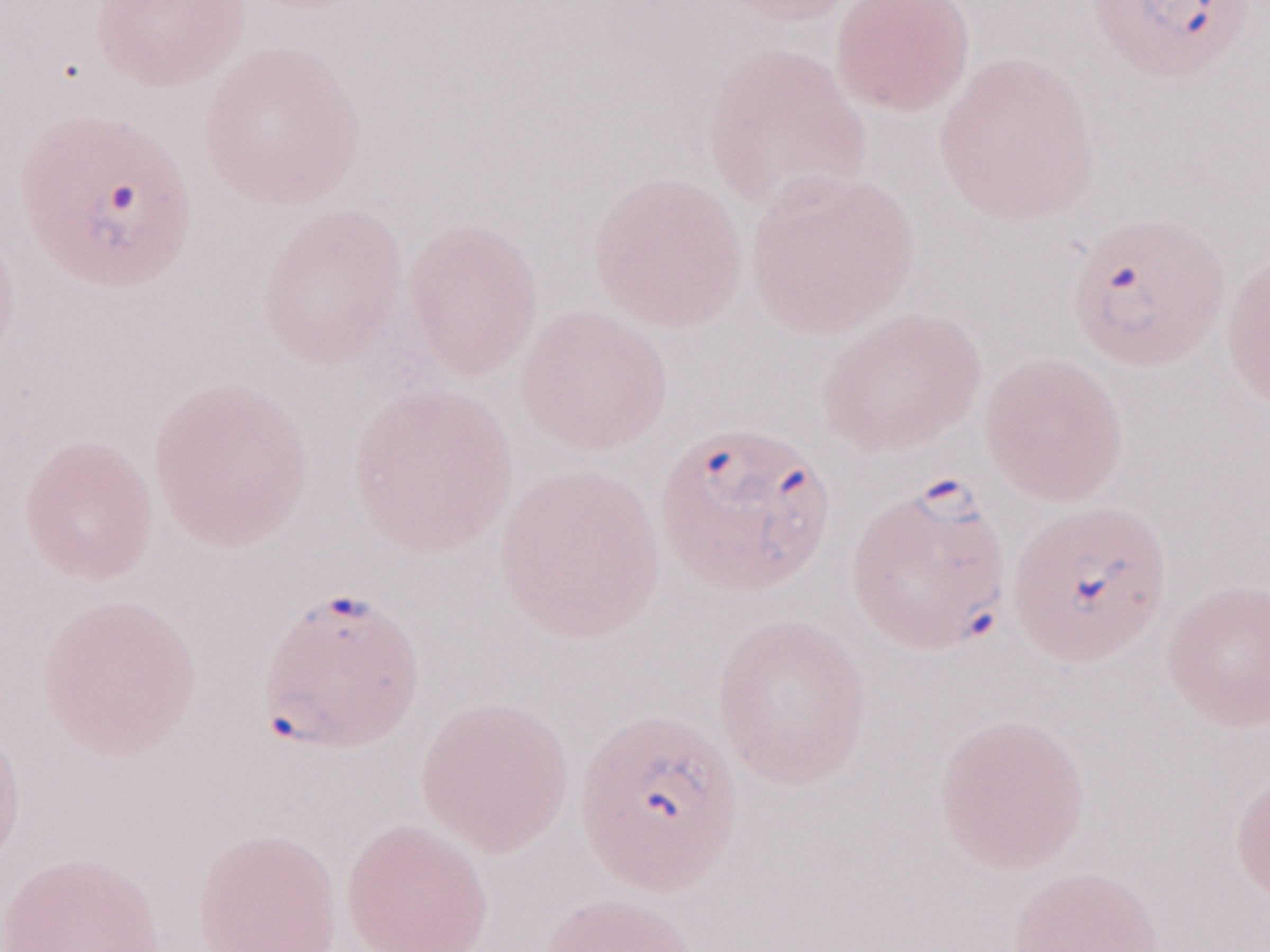
One field of this slide. May-Grünwald-Giemsa (MGG) stain. Patient-level malaria diagnosis: positive. Image is 1270×952 pixels. Magnification: 1,000x. Olympus BX43 microscope and DP73 digital camera. Thin peripheral-blood smear.